State the preparation type.
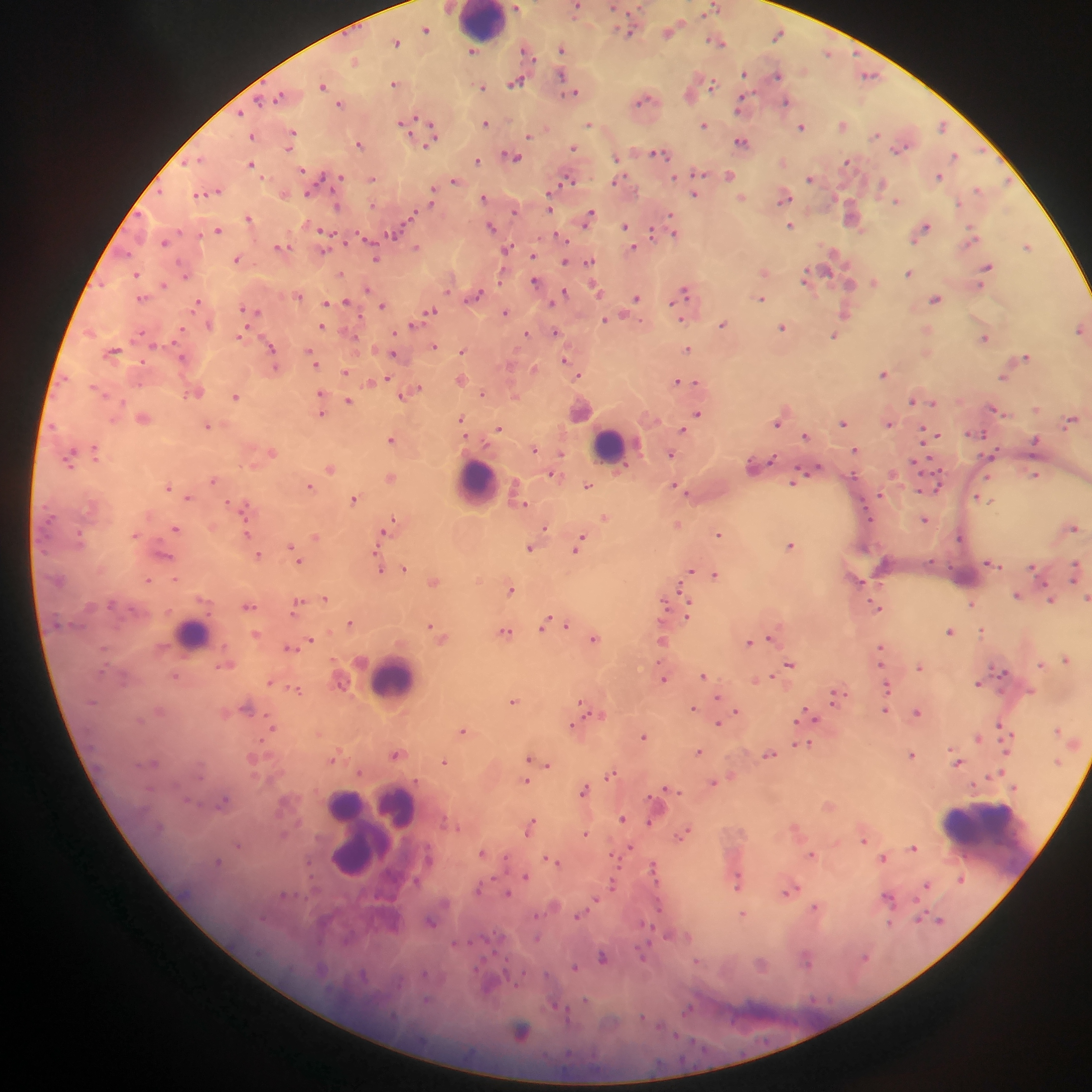

This is a thick smear.

capture = mobile-phone photograph through a microscope
leukocyte locations = approximate centers as (x, y) in pixels: (480, 22), (611, 445), (477, 482), (192, 634), (394, 679), (345, 804), (398, 806), (360, 816), (983, 843), (363, 849)
country = Ghana
field of view = single
image size = 1092×1092 pixels
malaria parasite locations = approximate centers as (x, y) in pixels: (516, 7), (613, 7), (639, 8), (577, 9), (714, 9), (705, 15), (426, 29), (669, 31), (778, 33), (631, 34), (397, 41), (721, 43), (561, 48), (473, 51), (527, 51), (827, 53), (355, 60), (744, 73), (870, 75), (561, 76), (777, 76), (395, 83), (516, 83), (712, 83), (323, 85), (483, 87), (575, 92), (280, 96), (689, 96), (643, 99), (786, 101), (340, 104), (740, 105), (240, 112), (485, 123), (403, 124), (589, 124), (704, 125), (843, 125), (942, 126), (802, 127), (433, 130), (293, 133), (877, 135), (529, 136), (252, 137), (741, 141), (359, 144), (574, 148), (899, 149), (658, 154), (513, 156), (955, 156), (616, 157), (196, 160), (478, 161), (847, 162), (252, 164), (302, 171), (701, 173), (729, 175), (675, 177), (939, 177), (339, 178), (810, 178), (374, 179), (567, 179), (454, 180), (615, 181), (881, 185), (978, 189), (432, 191), (308, 193), (201, 194), (695, 195), (484, 197), (743, 197), (785, 198), (896, 201), (550, 204), (337, 207), (514, 210), (590, 216), (248, 218), (671, 218), (852, 218), (791, 225), (625, 226), (490, 227), (924, 229), (218, 230), (325, 232), (652, 233), (674, 233), (971, 233), (394, 234), (561, 237), (164, 242), (1028, 246), (281, 247), (417, 247), (633, 248), (323, 250), (506, 250), (833, 251), (127, 253), (532, 255), (375, 258), (238, 259), (589, 261), (565, 262), (987, 267), (825, 271), (764, 272), (909, 273), (136, 275), (185, 275), (341, 275), (806, 277), (534, 281), (874, 283), (164, 284), (850, 284), (367, 289), (596, 289), (685, 292), (565, 293), (298, 295), (476, 296), (141, 298), (636, 298), (761, 299), (935, 299), (346, 301), (332, 302), (198, 303), (326, 303), (383, 306), (245, 310), (431, 311), (255, 312), (505, 313), (846, 313), (606, 319), (683, 319), (412, 324), (722, 325), (322, 326), (783, 328), (1079, 329), (555, 332), (526, 333), (240, 336), (834, 336), (984, 338), (435, 347), (272, 348), (687, 349), (462, 350), (113, 352), (311, 354), (394, 354), (183, 357), (1025, 357), (565, 360), (314, 361), (345, 372), (578, 374), (884, 374), (388, 378), (1004, 378), (461, 379), (676, 381), (685, 381), (696, 382), (413, 391), (196, 392), (483, 393), (321, 394), (235, 396), (405, 396), (912, 400), (349, 401), (934, 402), (1037, 408), (995, 409), (321, 412), (697, 413), (143, 418), (462, 418), (1071, 420), (777, 423), (844, 424), (889, 424), (207, 426), (498, 428), (683, 429), (925, 433), (974, 433), (804, 435), (933, 435), (391, 440), (1036, 441), (535, 449), (855, 450), (96, 452), (272, 452), (560, 454), (671, 454), (990, 455), (71, 457), (771, 459), (916, 461), (752, 465), (817, 468), (330, 469), (553, 474), (1034, 475), (390, 477), (212, 480), (795, 483), (588, 485), (310, 486), (936, 486), (169, 487), (675, 487), (880, 494), (188, 497), (354, 499), (983, 499), (521, 503), (243, 507), (604, 517), (924, 520), (392, 523), (677, 524), (545, 527), (1072, 527), (176, 528), (387, 530), (247, 534), (718, 534), (960, 536), (316, 537), (579, 545), (790, 545), (291, 548), (529, 548), (165, 555), (259, 555), (298, 560), (992, 564), (403, 568), (1032, 568), (380, 570), (690, 571), (1073, 571), (715, 575), (148, 580), (176, 580), (434, 582), (511, 589), (1017, 595), (326, 598), (1086, 599), (1050, 601), (664, 603), (971, 604), (297, 605), (248, 606), (876, 607), (689, 612), (350, 623), (544, 624), (431, 625), (565, 625), (505, 631), (949, 631), (982, 631), (771, 637), (594, 639), (310, 640), (661, 641), (749, 643), (288, 648), (879, 649), (1067, 659), (790, 663), (1041, 663), (921, 667), (703, 675), (176, 676), (766, 677), (663, 679), (759, 679), (270, 682), (978, 683), (888, 686), (297, 690), (718, 697), (835, 697), (513, 701), (582, 704), (246, 707), (693, 708), (736, 711), (885, 711), (917, 712), (806, 713), (594, 714), (718, 723), (1000, 726), (272, 727), (572, 728), (1058, 729), (464, 731), (643, 736), (977, 738), (807, 744), (698, 752), (769, 754), (396, 755), (913, 755), (335, 758), (529, 758), (958, 761), (154, 762), (444, 762), (547, 765), (611, 773), (1000, 773), (526, 781), (714, 782), (584, 789), (669, 789), (223, 802), (621, 818), (650, 822), (530, 825), (684, 833), (586, 834), (864, 840), (239, 846), (630, 847), (913, 848), (481, 852), (812, 855), (883, 858), (550, 859), (217, 862), (654, 866), (525, 876), (961, 879), (737, 882), (613, 884), (927, 885), (479, 889), (791, 890), (507, 893), (889, 898), (595, 900), (660, 906), (815, 908), (579, 914), (743, 914), (919, 918), (940, 920), (431, 921), (537, 938), (644, 954), (602, 957), (865, 958), (806, 960), (575, 967), (490, 988), (586, 1001), (558, 1007), (688, 1009), (566, 1013), (643, 1018), (522, 1032)